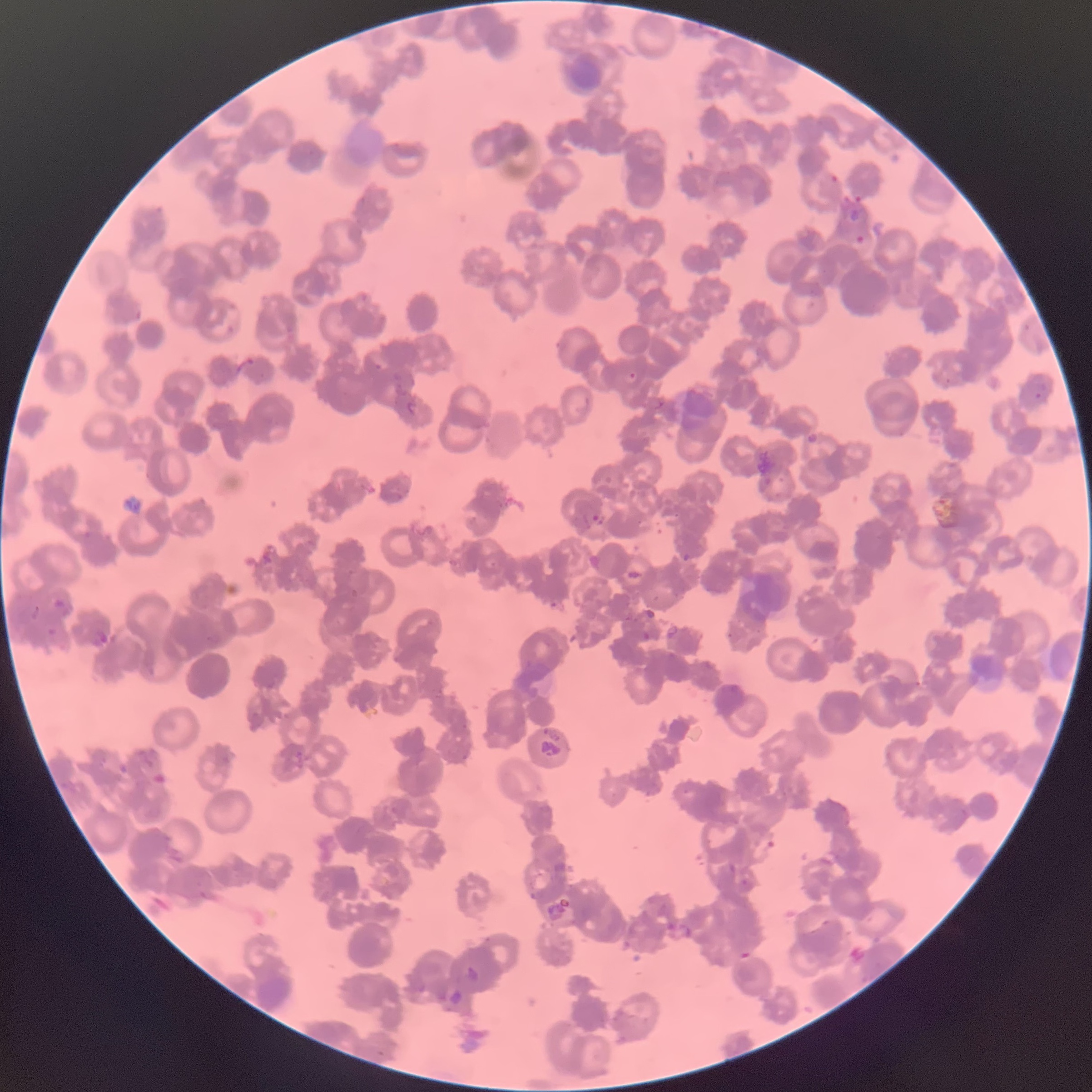
Summary:
  - Coordinate format: approximate bounding boxes as (x1, y1, x2, y2) in pixels
  - Plasmodium parasite locations: (830, 175, 838, 184), (841, 196, 865, 207), (855, 234, 868, 245), (371, 356, 390, 371), (626, 371, 636, 382), (944, 377, 952, 384), (1032, 392, 1043, 400), (807, 433, 818, 444), (761, 478, 774, 486), (591, 514, 599, 521), (682, 552, 691, 562), (54, 598, 65, 608), (30, 605, 41, 619), (47, 627, 59, 636), (642, 631, 652, 640), (727, 632, 735, 639), (145, 759, 154, 769), (740, 879, 749, 890)
  - Modality: light microscopy
  - Image size: 1092×1092 pixels
  - Red blood cell morphology: rouleaux formation
  - Preparation: thin blood smear